Assess the morphology of the erythrocytes.
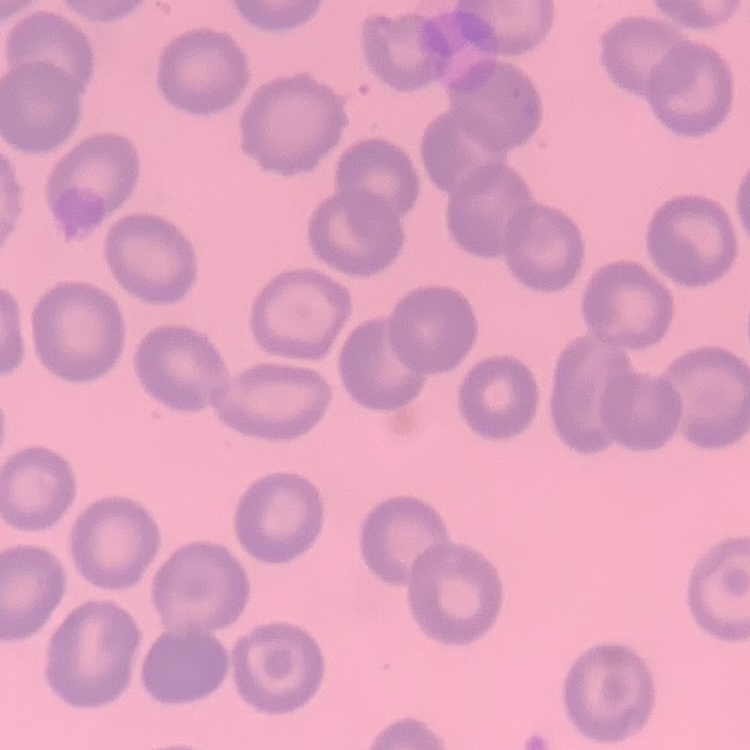
They show no rouleaux formation.

{
  "preparation": "thin peripheral smear",
  "image_type": "square crop of a larger photomicrograph",
  "stain": "Field's or Giemsa"
}